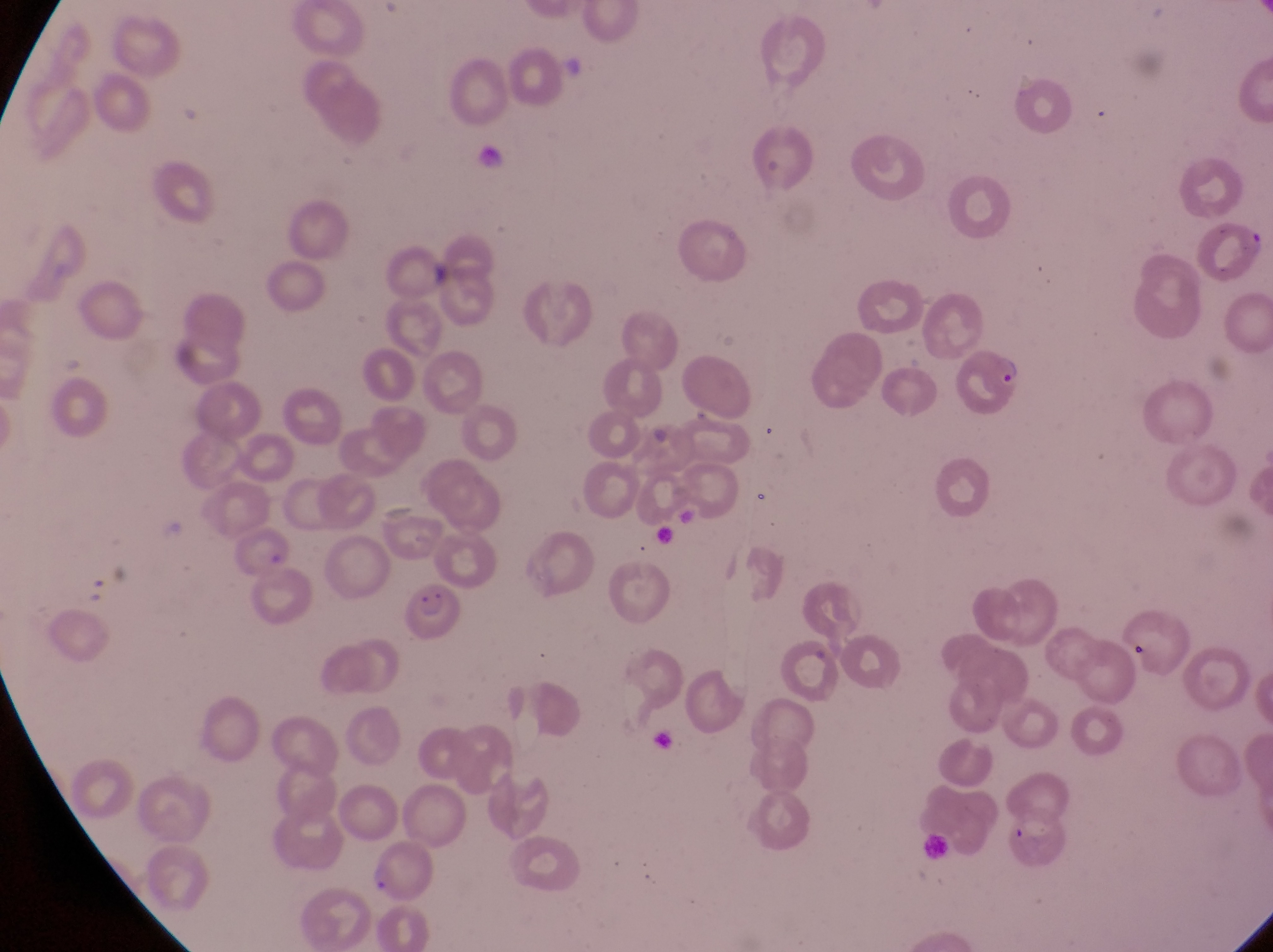
Approximate bounding boxes as (left, top, right, bottom) in pixels. Parasitised red blood cell locations: (958, 344, 1027, 414), (405, 577, 462, 645). Captured by a smartphone held over the eyepiece of an Olympus CX-23 microscope. Single field of view. Thin blood film. Collected in Uganda. At a magnification of 1000x. Image is 1273×952 pixels.